Point out each Plasmodium parasite.
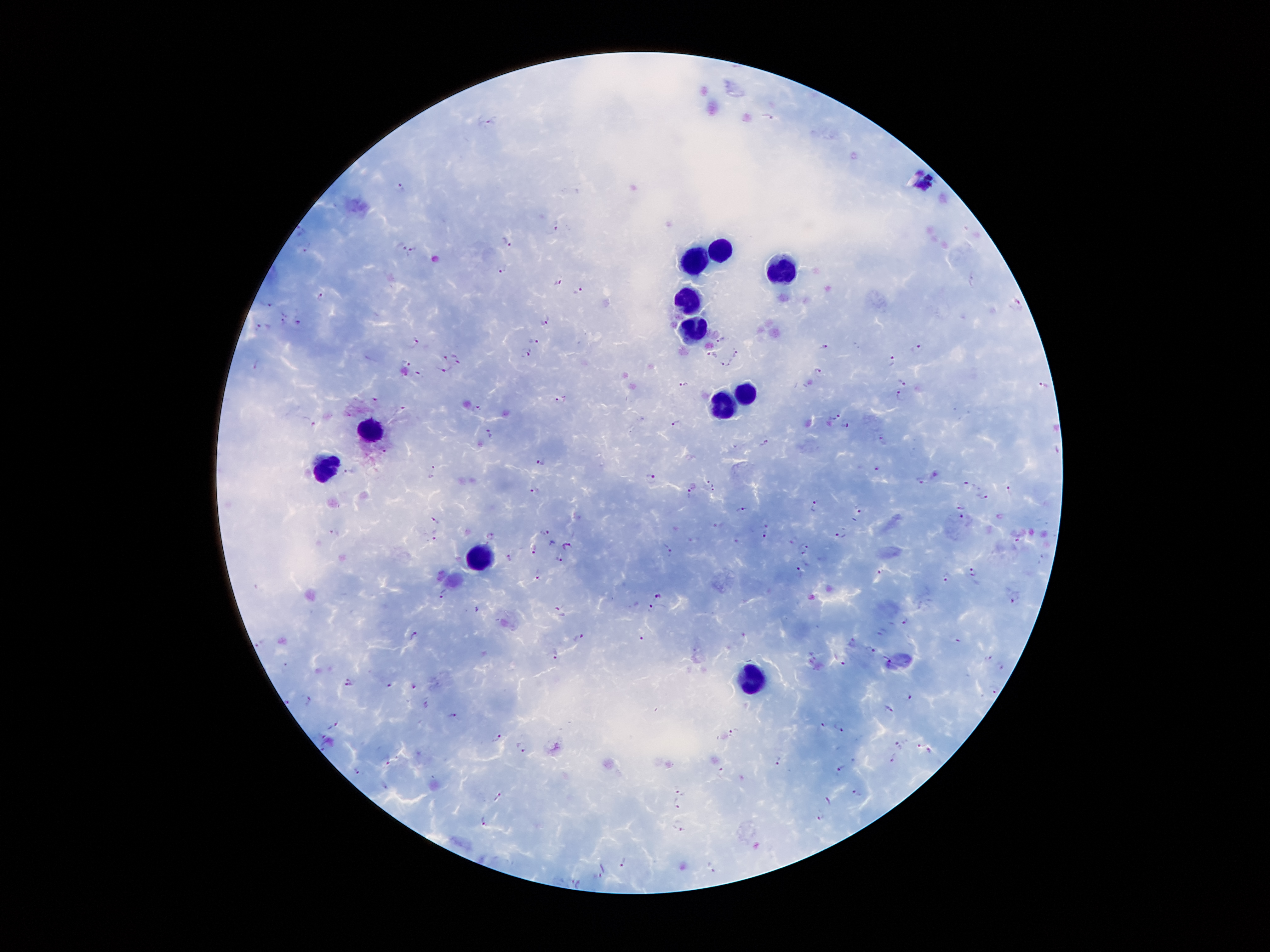

Approximate object centers, in pixels from the top-left corner.
Plasmodium parasites: (x=768, y=116), (x=491, y=122), (x=402, y=187), (x=558, y=227), (x=302, y=229), (x=507, y=239), (x=402, y=244), (x=306, y=249), (x=412, y=252), (x=503, y=270), (x=558, y=283), (x=579, y=292), (x=321, y=297), (x=270, y=302), (x=1018, y=307), (x=284, y=316), (x=300, y=320), (x=546, y=321), (x=263, y=327), (x=721, y=336), (x=416, y=339), (x=536, y=341), (x=827, y=346), (x=918, y=349), (x=737, y=352), (x=527, y=354), (x=712, y=355), (x=443, y=356), (x=458, y=358), (x=894, y=360), (x=406, y=362), (x=258, y=365), (x=727, y=367), (x=447, y=370), (x=819, y=371), (x=418, y=373), (x=903, y=380), (x=685, y=384), (x=1045, y=385), (x=900, y=394), (x=378, y=399), (x=561, y=399), (x=476, y=408), (x=402, y=409), (x=835, y=416), (x=309, y=420), (x=676, y=422), (x=846, y=424), (x=488, y=431), (x=882, y=440), (x=767, y=442), (x=383, y=448), (x=542, y=462), (x=876, y=467), (x=432, y=471), (x=350, y=473), (x=936, y=474), (x=651, y=477), (x=706, y=481), (x=922, y=481), (x=966, y=484), (x=714, y=487), (x=1010, y=490), (x=534, y=491), (x=689, y=494), (x=985, y=494), (x=814, y=505), (x=961, y=507), (x=742, y=508), (x=860, y=508), (x=963, y=517), (x=437, y=520), (x=764, y=521), (x=719, y=522), (x=336, y=531), (x=842, y=531), (x=544, y=533), (x=434, y=534), (x=490, y=534), (x=765, y=534), (x=1017, y=538), (x=736, y=541), (x=552, y=543), (x=567, y=545), (x=806, y=545), (x=535, y=547), (x=669, y=549), (x=802, y=551), (x=560, y=557), (x=510, y=558), (x=976, y=570), (x=801, y=571), (x=881, y=571), (x=537, y=573), (x=946, y=579), (x=444, y=593), (x=658, y=594), (x=1015, y=599), (x=651, y=605), (x=479, y=608), (x=559, y=612), (x=905, y=618), (x=882, y=631), (x=413, y=634), (x=580, y=637), (x=643, y=638), (x=956, y=638), (x=261, y=641), (x=853, y=641), (x=872, y=649), (x=555, y=651), (x=989, y=657), (x=845, y=661), (x=889, y=662), (x=287, y=664), (x=1001, y=665), (x=347, y=682), (x=389, y=683), (x=415, y=685), (x=994, y=691), (x=909, y=696), (x=308, y=698), (x=887, y=708), (x=454, y=714), (x=822, y=724), (x=335, y=725), (x=840, y=726), (x=733, y=734), (x=498, y=736), (x=900, y=744), (x=523, y=747), (x=892, y=759), (x=390, y=760), (x=779, y=760), (x=841, y=768), (x=357, y=770), (x=721, y=773), (x=385, y=786), (x=680, y=791), (x=858, y=791), (x=500, y=795), (x=677, y=803), (x=821, y=815), (x=486, y=819), (x=679, y=825), (x=625, y=861), (x=712, y=867), (x=599, y=876), (x=576, y=882).

Summary:
  - Leukocyte locations: (x=719, y=247), (x=695, y=260), (x=785, y=271), (x=688, y=294), (x=691, y=328), (x=746, y=387), (x=724, y=402), (x=367, y=428), (x=330, y=470), (x=481, y=560), (x=758, y=678)
  - Stain: Giemsa
  - Image size: 1270×952 pixels
  - Field of view: one from this slide
  - Patient malaria status: positive for Plasmodium falciparum
  - Capture: smartphone camera through the microscope eyepiece
  - Magnification: 100x
  - Preparation: thick peripheral-blood smear